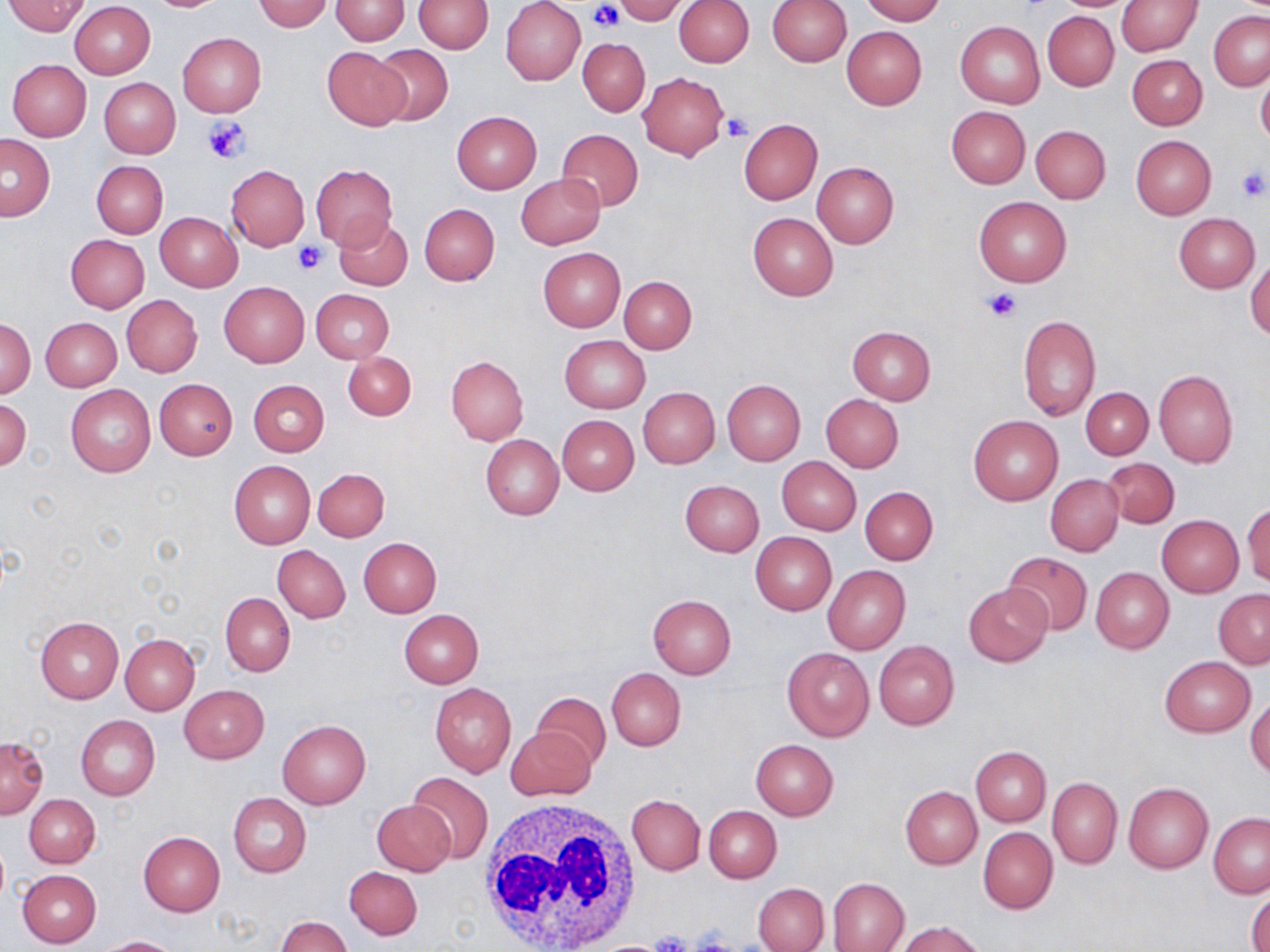
Approximate bounding boxes as (x1,y1)-(x2,y2) corner pairs in pixels. White blood cell locations: (475,797)-(643,952). Uninfected red blood cell locations (subset): (331,0)-(409,44), (415,0)-(493,53), (613,0)-(687,24), (768,0)-(852,66), (859,0)-(943,23), (1050,0)-(1141,12), (3,1)-(90,36), (140,1)-(231,12), (254,1)-(333,32), (501,1)-(586,85), (673,1)-(754,67), (1116,1)-(1202,56), (69,2)-(155,79), (1043,11)-(1119,90), (1208,11)-(1270,90), (955,21)-(1044,107), (842,26)-(927,109), (177,33)-(266,117), (577,38)-(650,115), (369,45)-(453,127), (322,46)-(412,130), (1127,55)-(1207,130), (7,59)-(91,141), (1256,70)-(1270,150), (637,72)-(730,159), (99,77)-(180,158), (946,106)-(1030,188), (451,111)-(541,194), (738,118)-(823,204), (1030,124)-(1111,203), (556,128)-(643,212), (1,134)-(55,221), (1131,135)-(1216,219), (92,161)-(168,239), (812,162)-(898,247), (310,163)-(397,249), (225,165)-(310,250), (515,173)-(606,249), (973,197)-(1071,286), (419,203)-(499,285), (155,212)-(242,291), (748,212)-(838,301), (1174,212)-(1260,292), (333,215)-(413,290), (65,234)-(149,313), (538,248)-(625,331), (1246,258)-(1270,339), (619,275)-(697,353), (219,281)-(310,367), (311,288)-(393,364), (122,295)-(202,377), (1017,315)-(1100,420), (41,316)-(122,391), (2,319)-(35,397), (847,325)-(936,405), (559,336)-(650,414), (343,351)-(416,420), (446,355)-(528,445), (1153,367)-(1238,468), (154,378)-(237,459), (249,379)-(329,456), (722,380)-(806,465), (66,384)-(155,477), (638,387)-(720,469), (1081,387)-(1153,459), (821,394)-(903,472), (0,397)-(32,471), (557,415)-(638,495), (969,415)-(1063,505), (480,434)-(564,519), (777,457)-(861,535), (1103,458)-(1180,528), (230,460)-(315,548), (314,468)-(390,541), (1045,473)-(1123,556), (679,480)-(764,556), (860,486)-(938,565), (1242,504)-(1270,587), (1157,515)-(1244,598), (750,532)-(837,615), (359,537)-(442,616), (273,544)-(350,623), (1002,551)-(1092,636), (823,565)-(911,654), (1090,566)-(1174,654), (962,583)-(1054,667), (1213,589)-(1270,669), (220,593)-(295,676), (648,595)-(736,679), (400,610)-(483,687), (36,617)-(124,703), (120,632)-(200,714), (874,641)-(960,730), (783,647)-(873,741), (1160,656)-(1255,736), (607,667)-(686,751), (430,682)-(517,776), (179,684)-(269,764), (531,693)-(612,771), (1246,695)-(1270,779), (75,714)-(160,801), (277,719)-(370,809), (507,726)-(596,801), (0,736)-(48,818), (751,739)-(838,820), (970,746)-(1051,825), (406,771)-(494,865), (1048,778)-(1121,868), (1122,782)-(1214,873), (900,786)-(982,868), (228,793)-(311,878), (24,794)-(100,868), (627,795)-(704,875), (372,800)-(455,875), (704,805)-(781,883), (1209,812)-(1270,897), (978,828)-(1057,913), (138,832)-(225,917), (345,866)-(421,940), (17,869)-(101,947), (828,877)-(909,951), (753,882)-(829,952), (1248,889)-(1270,952), (277,916)-(353,952), (898,921)-(986,952), (96,936)-(179,951). Platelet locations (subset): (590,1)-(622,34), (721,112)-(753,142), (202,117)-(250,165), (1235,167)-(1268,203), (294,242)-(328,273), (981,287)-(1020,322), (690,929)-(738,952), (647,932)-(693,952). Slide-level diagnosis: no evidence of blood parasites. Thin blood smear. 1000x magnification. Light microscopy. May-Grünwald-Giemsa-stained preparation. One field of a larger specimen. Image is 1270×952 pixels.